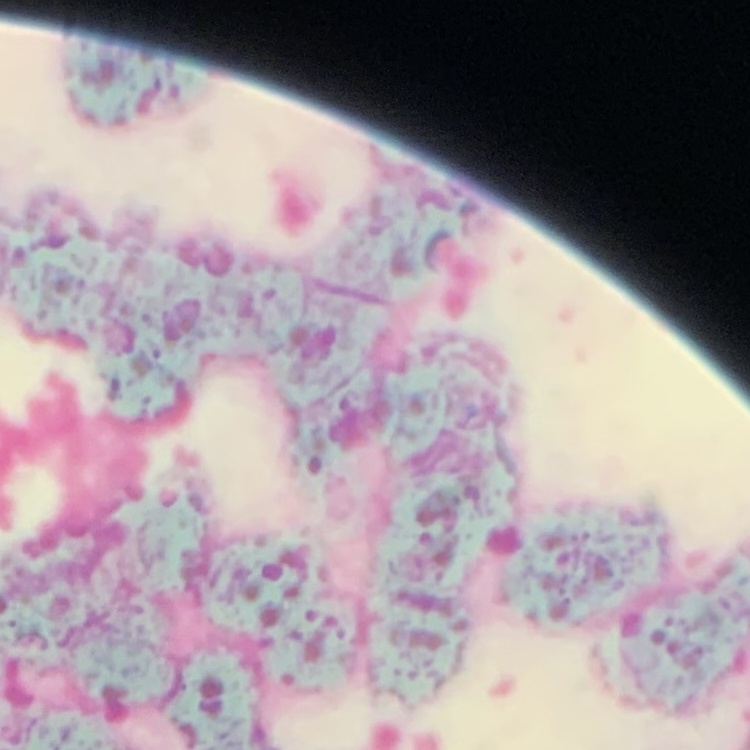

red_blood_cell_morphology: rouleaux formation
stain: Field's or Giemsa
image_type: square crop of a larger photomicrograph
preparation: thin peripheral smear